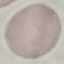
{
  "result": "no malaria parasites detected",
  "stain": "Giemsa",
  "capture": "smartphone camera at the microscope eyepiece",
  "image_type": "cell patch, automatically extracted from a larger field of view and resized to 64 × 64 pixels",
  "preparation": "thin blood film"
}